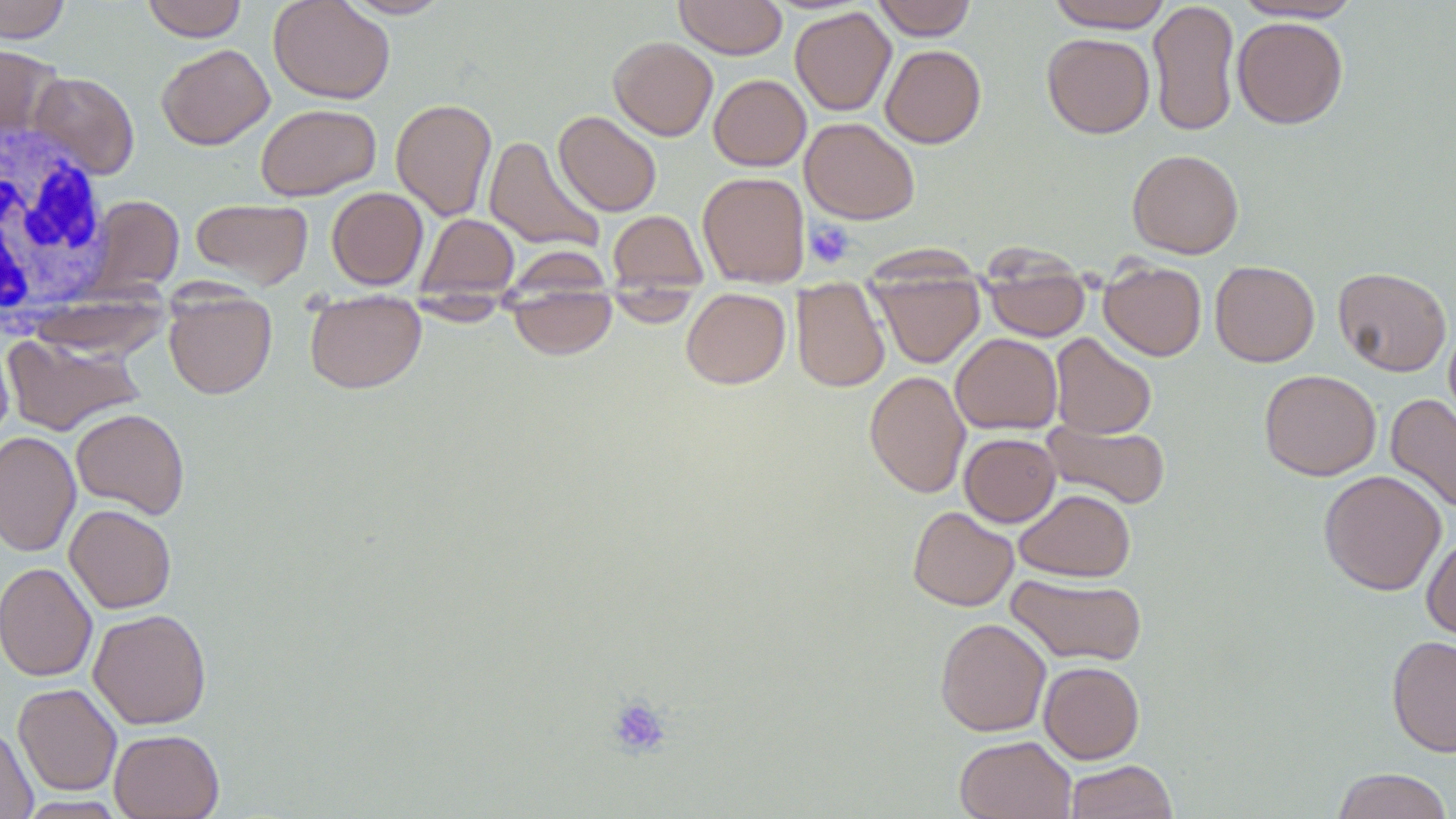
Summary:
  - Coordinate format: approximate bounding boxes as named x1/y1/x2/y2 corners in pixels
  - White blood cell locations: (x1=0, y1=120, x2=113, y2=326)
  - Uninfected red blood cell locations: (x1=0, y1=0, x2=71, y2=43), (x1=140, y1=0, x2=248, y2=42), (x1=268, y1=0, x2=395, y2=104), (x1=339, y1=0, x2=452, y2=19), (x1=674, y1=0, x2=788, y2=59), (x1=871, y1=0, x2=977, y2=40), (x1=1046, y1=0, x2=1174, y2=32), (x1=1232, y1=0, x2=1363, y2=22), (x1=1148, y1=1, x2=1240, y2=137), (x1=790, y1=7, x2=896, y2=116), (x1=1232, y1=17, x2=1348, y2=129), (x1=1042, y1=33, x2=1154, y2=138), (x1=609, y1=37, x2=718, y2=141), (x1=0, y1=43, x2=62, y2=142), (x1=156, y1=43, x2=274, y2=149), (x1=880, y1=44, x2=986, y2=148), (x1=29, y1=71, x2=140, y2=179), (x1=709, y1=74, x2=811, y2=171), (x1=390, y1=98, x2=497, y2=220), (x1=255, y1=103, x2=381, y2=200), (x1=553, y1=111, x2=662, y2=217), (x1=800, y1=117, x2=920, y2=224), (x1=483, y1=135, x2=605, y2=253), (x1=1127, y1=149, x2=1244, y2=259), (x1=697, y1=171, x2=810, y2=286), (x1=326, y1=187, x2=429, y2=290), (x1=86, y1=195, x2=184, y2=296), (x1=190, y1=198, x2=313, y2=288), (x1=607, y1=210, x2=708, y2=293), (x1=417, y1=213, x2=519, y2=301), (x1=1099, y1=261, x2=1206, y2=361), (x1=1210, y1=261, x2=1320, y2=366), (x1=983, y1=263, x2=1091, y2=341), (x1=1332, y1=266, x2=1452, y2=377), (x1=870, y1=269, x2=986, y2=369), (x1=791, y1=279, x2=890, y2=392), (x1=506, y1=283, x2=617, y2=360), (x1=604, y1=287, x2=701, y2=328), (x1=681, y1=288, x2=791, y2=389), (x1=164, y1=289, x2=277, y2=399), (x1=304, y1=295, x2=426, y2=394), (x1=402, y1=297, x2=515, y2=326), (x1=1444, y1=319, x2=1456, y2=429), (x1=2, y1=333, x2=146, y2=436), (x1=950, y1=333, x2=1063, y2=434), (x1=1050, y1=333, x2=1156, y2=439), (x1=1259, y1=369, x2=1381, y2=481), (x1=864, y1=370, x2=971, y2=499), (x1=1386, y1=393, x2=1456, y2=515), (x1=71, y1=407, x2=190, y2=519), (x1=1043, y1=420, x2=1170, y2=510), (x1=0, y1=430, x2=81, y2=558), (x1=960, y1=433, x2=1060, y2=527), (x1=1319, y1=469, x2=1446, y2=596), (x1=1015, y1=488, x2=1135, y2=582), (x1=64, y1=504, x2=176, y2=613), (x1=907, y1=506, x2=1019, y2=611), (x1=1422, y1=532, x2=1456, y2=643), (x1=0, y1=562, x2=97, y2=682), (x1=1006, y1=574, x2=1148, y2=666), (x1=88, y1=608, x2=212, y2=729), (x1=934, y1=617, x2=1051, y2=736), (x1=1387, y1=634, x2=1456, y2=757), (x1=1038, y1=661, x2=1144, y2=764), (x1=13, y1=683, x2=122, y2=796), (x1=0, y1=724, x2=37, y2=819), (x1=109, y1=728, x2=224, y2=818), (x1=954, y1=735, x2=1076, y2=819), (x1=1065, y1=759, x2=1177, y2=819), (x1=1330, y1=767, x2=1454, y2=819), (x1=14, y1=796, x2=128, y2=818)
  - Platelet locations: (x1=804, y1=219, x2=855, y2=269), (x1=605, y1=695, x2=672, y2=759)
  - Slide-level diagnosis: negative for blood parasites
  - Field of view: single
  - Preparation: thin blood film
  - Image size: 1456×819 pixels
  - Modality: light microscopy
  - Stain: May-Grünwald-Giemsa
  - Magnification: 1000x